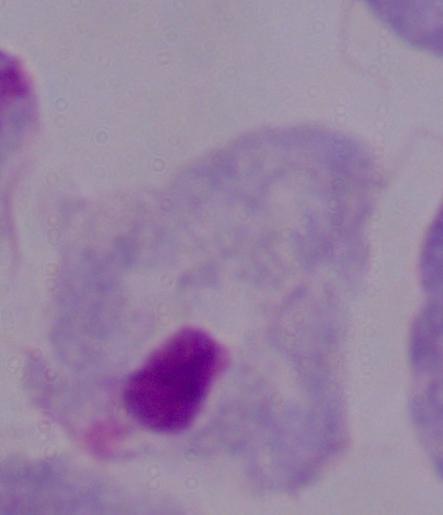
Summary:
  - Identification: trichomonad
  - Magnification: 1000x
  - Modality: photomicrograph